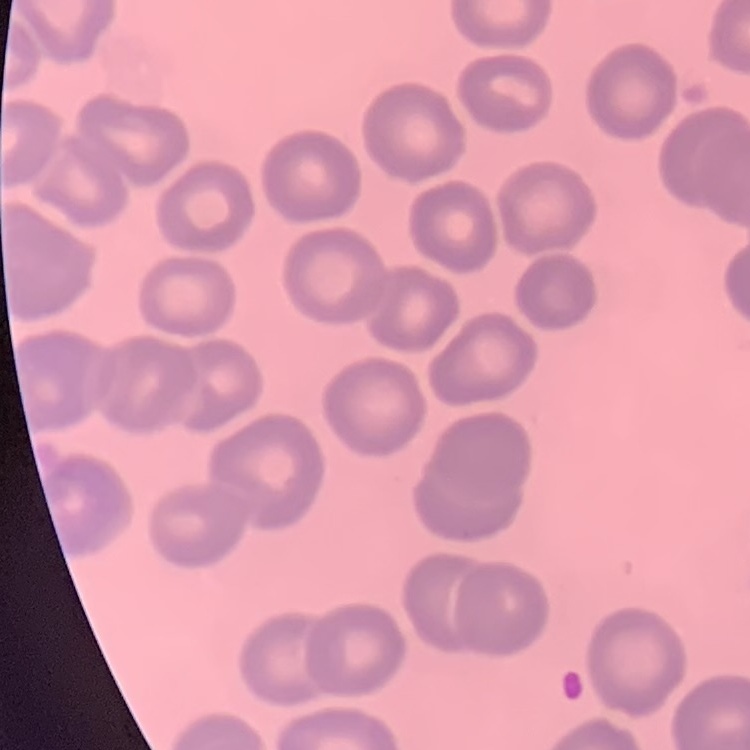 The erythrocytes show no rouleaux formation. Field's or Giemsa stain. Thin peripheral smear. Square crop of a larger photomicrograph.